Give the extent of all uninfected red blood cells.
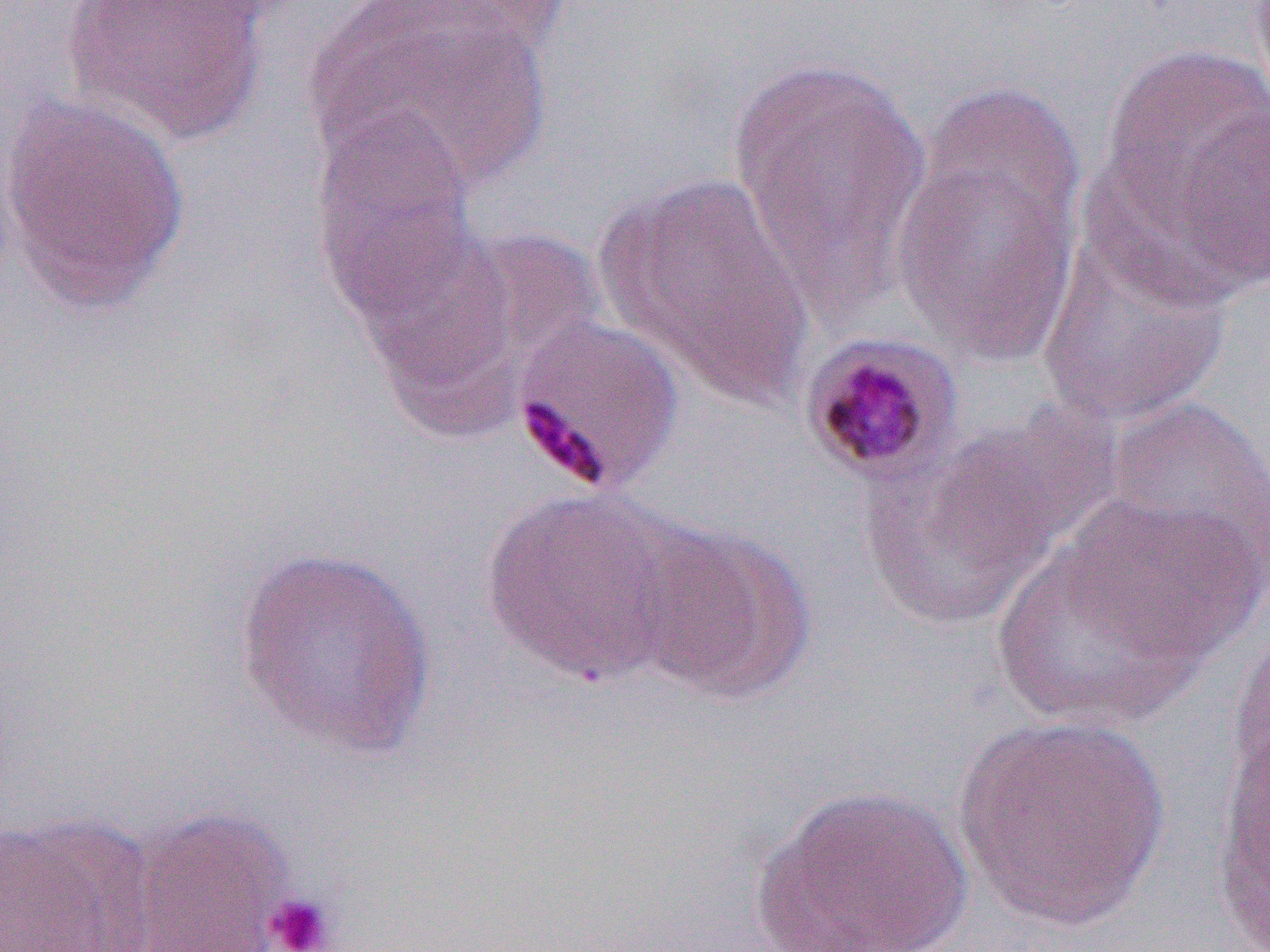

Approximate bounding boxes as (x1,y1)-(x2,y2) corner pairs in pixels.
Uninfected red blood cells: (63,0)-(273,146), (306,2)-(556,195), (1100,41)-(1269,276), (727,55)-(933,310), (0,93)-(193,315), (889,96)-(1084,371), (1171,104)-(1270,294), (308,112)-(480,324), (596,173)-(815,408), (1036,229)-(1233,427), (1106,397)-(1270,579), (859,426)-(1084,632), (479,487)-(696,687), (1057,494)-(1267,664), (997,518)-(1234,728), (627,520)-(816,703), (234,542)-(441,760), (1229,623)-(1270,793), (1211,713)-(1269,952), (953,714)-(1170,931), (751,783)-(973,952), (123,808)-(295,951), (0,812)-(157,952).

slide-level diagnosis = Plasmodium malariae
preparation = thin blood smear
image size = 1270×952 pixels
platelet locations (subset) = approximate bounding boxes as (x1,y1)-(x2,y2) corner pairs in pixels: (263,892)-(339,952)
magnification = 1000x
modality = optical microscopy
field of view = single